State which parasite is depicted.
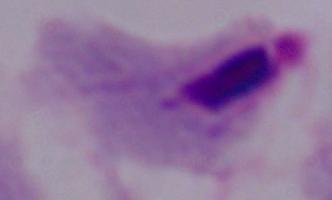

A trichomonad.

Summary:
  - Magnification: 1000x
  - Modality: photomicrograph